State the preparation type.
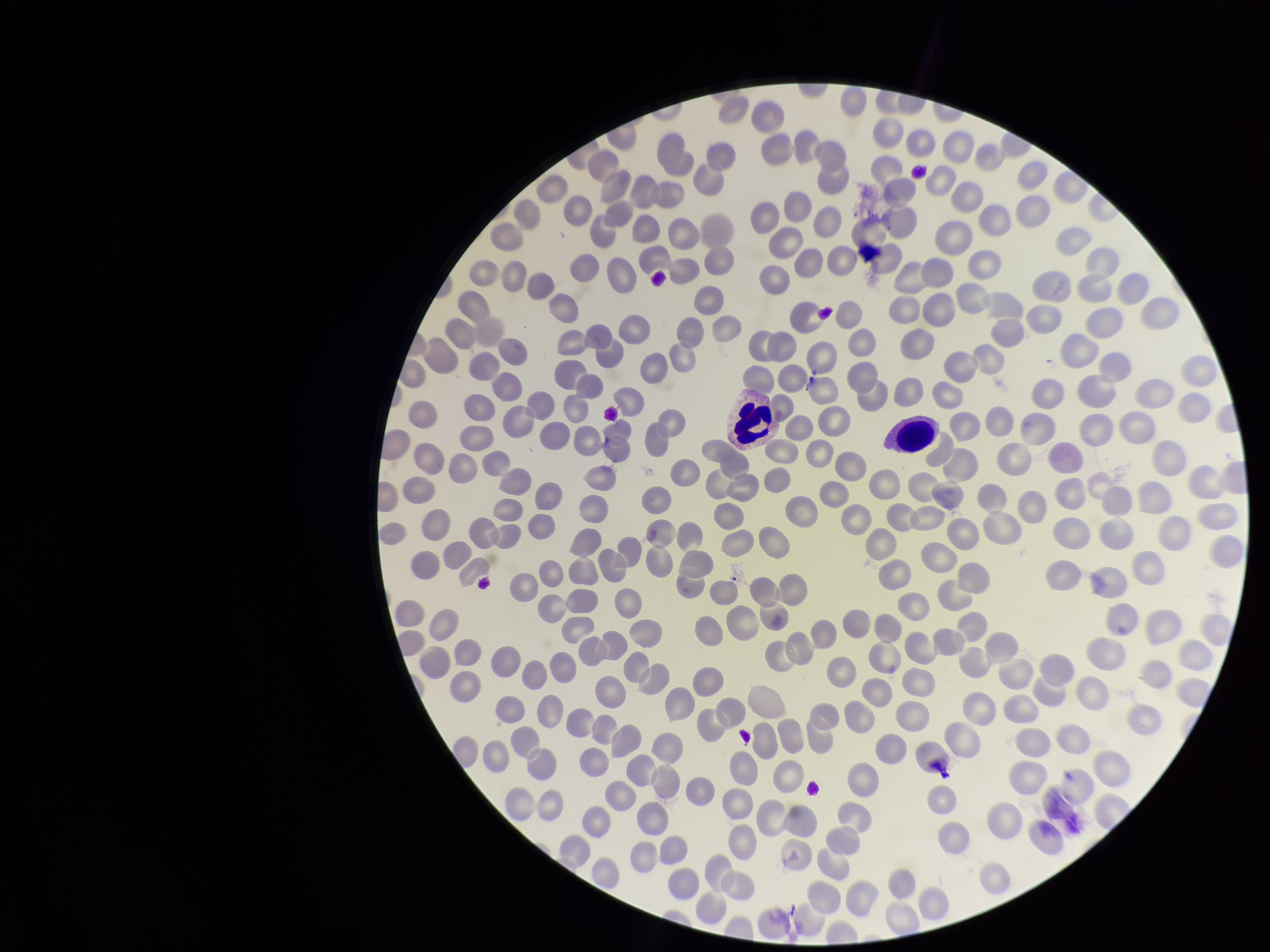

Thin.

Summary:
  - Field of view: single
  - Stain: Giemsa
  - Red blood cell count: 300
  - Image size: 1270×952 pixels
  - Patient malaria status: negative
  - Capture: smartphone photograph through the microscope eyepiece
  - Parasitized red blood cells: none detected
  - Parasitized red blood cell count: 0